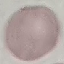

Summary:
  - Malaria status: uninfected
  - Stain: Giemsa
  - Image type: automatically extracted cell patch, resized to 64 × 64 pixels
  - Capture: smartphone camera at the microscope eyepiece
  - Preparation: thin blood film